Assess the morphology of the red blood cells.
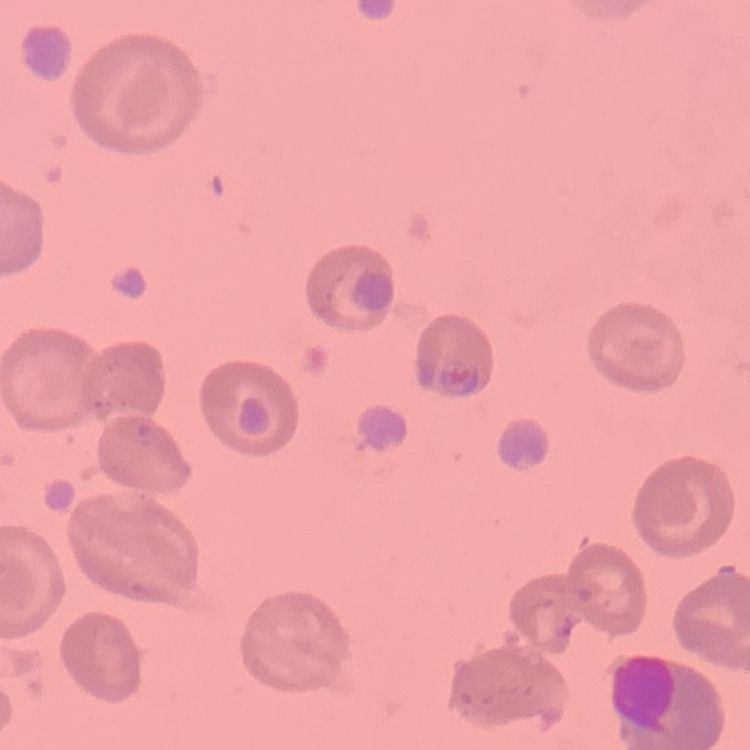
They show no rouleaux formation.

stain: Field's or Giemsa
preparation: thin blood smear
image_type: one tile cut from a larger photomicrograph